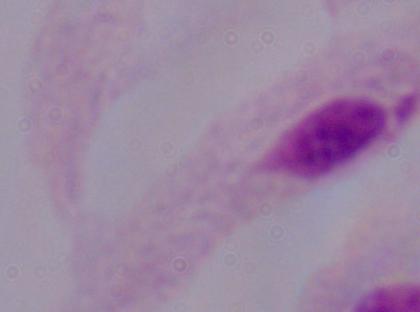
Summary:
  - Magnification: 1000x
  - Identification: trichomonad
  - Modality: photomicrograph